Locate every blood parasite and identify its species.
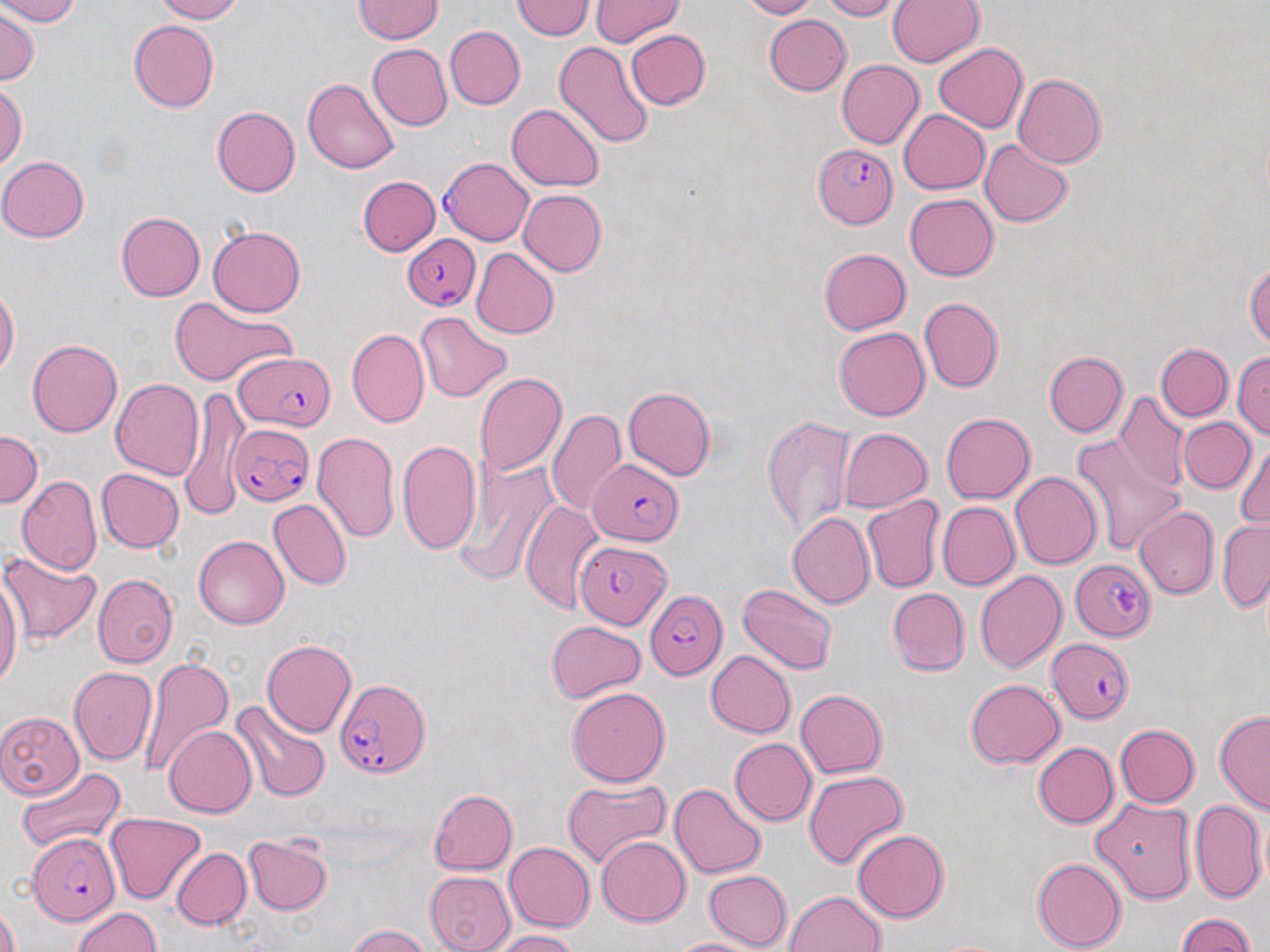

Approximate bounding boxes as named x1/y1/x2/y2 corners in pixels.
Plasmodium falciparum-infected red blood cells: (x1=813, y1=140, x2=898, y2=231), (x1=439, y1=157, x2=533, y2=247), (x1=401, y1=231, x2=481, y2=312), (x1=232, y1=350, x2=339, y2=432), (x1=230, y1=422, x2=314, y2=505), (x1=587, y1=460, x2=683, y2=544), (x1=576, y1=533, x2=680, y2=631), (x1=1070, y1=559, x2=1156, y2=640), (x1=648, y1=589, x2=727, y2=680), (x1=1046, y1=637, x2=1134, y2=725), (x1=339, y1=674, x2=433, y2=779), (x1=26, y1=831, x2=119, y2=925).
No Plasmodium ovale, Plasmodium malariae, Plasmodium vivax, Babesia divergens, or Trypanosoma brucei observed.

Summary:
  - Uninfected red blood cell locations: (x1=0, y1=0, x2=84, y2=27), (x1=151, y1=0, x2=249, y2=23), (x1=354, y1=0, x2=443, y2=44), (x1=592, y1=0, x2=683, y2=46), (x1=738, y1=0, x2=820, y2=18), (x1=819, y1=0, x2=899, y2=20), (x1=888, y1=0, x2=985, y2=68), (x1=511, y1=1, x2=593, y2=41), (x1=0, y1=8, x2=40, y2=85), (x1=764, y1=14, x2=851, y2=96), (x1=128, y1=20, x2=219, y2=111), (x1=444, y1=26, x2=526, y2=109), (x1=625, y1=29, x2=711, y2=110), (x1=550, y1=40, x2=655, y2=149), (x1=366, y1=43, x2=451, y2=131), (x1=932, y1=43, x2=1029, y2=133), (x1=835, y1=60, x2=925, y2=149), (x1=1011, y1=74, x2=1105, y2=168), (x1=302, y1=78, x2=399, y2=175), (x1=0, y1=83, x2=26, y2=171), (x1=507, y1=101, x2=605, y2=191), (x1=215, y1=106, x2=301, y2=198), (x1=897, y1=108, x2=990, y2=194), (x1=979, y1=139, x2=1072, y2=227), (x1=0, y1=154, x2=90, y2=243), (x1=359, y1=176, x2=439, y2=256), (x1=517, y1=189, x2=608, y2=277), (x1=905, y1=194, x2=999, y2=280), (x1=115, y1=212, x2=205, y2=301), (x1=208, y1=226, x2=307, y2=317), (x1=470, y1=247, x2=560, y2=340), (x1=818, y1=248, x2=911, y2=335), (x1=1245, y1=257, x2=1270, y2=351), (x1=0, y1=285, x2=18, y2=380), (x1=168, y1=296, x2=295, y2=387), (x1=917, y1=297, x2=1003, y2=393), (x1=417, y1=313, x2=512, y2=400), (x1=834, y1=327, x2=930, y2=421), (x1=346, y1=328, x2=429, y2=428), (x1=28, y1=339, x2=122, y2=438), (x1=1157, y1=343, x2=1234, y2=422), (x1=1232, y1=348, x2=1270, y2=441), (x1=1044, y1=350, x2=1127, y2=436), (x1=473, y1=372, x2=565, y2=477), (x1=109, y1=377, x2=207, y2=480), (x1=622, y1=386, x2=716, y2=481), (x1=177, y1=391, x2=250, y2=519), (x1=1113, y1=391, x2=1190, y2=491), (x1=546, y1=406, x2=625, y2=516), (x1=941, y1=413, x2=1035, y2=505), (x1=761, y1=415, x2=856, y2=541), (x1=1178, y1=416, x2=1255, y2=492), (x1=837, y1=428, x2=930, y2=512), (x1=311, y1=429, x2=400, y2=547), (x1=0, y1=431, x2=42, y2=511), (x1=1073, y1=434, x2=1184, y2=556), (x1=397, y1=438, x2=482, y2=553), (x1=1233, y1=439, x2=1269, y2=533), (x1=454, y1=459, x2=563, y2=585), (x1=96, y1=469, x2=183, y2=553), (x1=1010, y1=471, x2=1102, y2=570), (x1=17, y1=473, x2=102, y2=572), (x1=860, y1=496, x2=944, y2=594), (x1=521, y1=499, x2=604, y2=617), (x1=267, y1=500, x2=351, y2=591), (x1=936, y1=502, x2=1019, y2=591), (x1=1135, y1=506, x2=1219, y2=600), (x1=787, y1=512, x2=874, y2=609), (x1=1217, y1=518, x2=1270, y2=614), (x1=193, y1=535, x2=289, y2=628), (x1=0, y1=546, x2=102, y2=644), (x1=0, y1=567, x2=22, y2=694), (x1=974, y1=570, x2=1065, y2=675), (x1=93, y1=574, x2=176, y2=665), (x1=735, y1=582, x2=838, y2=675), (x1=887, y1=588, x2=970, y2=675), (x1=546, y1=620, x2=645, y2=701), (x1=261, y1=638, x2=357, y2=738), (x1=706, y1=650, x2=796, y2=739), (x1=137, y1=656, x2=235, y2=779), (x1=69, y1=666, x2=156, y2=766), (x1=963, y1=678, x2=1063, y2=769), (x1=567, y1=685, x2=672, y2=786), (x1=795, y1=689, x2=889, y2=778), (x1=232, y1=700, x2=330, y2=802), (x1=0, y1=709, x2=83, y2=799), (x1=1214, y1=711, x2=1269, y2=811), (x1=164, y1=724, x2=257, y2=819), (x1=1114, y1=724, x2=1199, y2=807), (x1=728, y1=738, x2=814, y2=825), (x1=1032, y1=741, x2=1118, y2=829), (x1=15, y1=765, x2=127, y2=855), (x1=802, y1=769, x2=909, y2=872), (x1=562, y1=779, x2=673, y2=868), (x1=670, y1=783, x2=766, y2=879), (x1=426, y1=787, x2=518, y2=875), (x1=1090, y1=796, x2=1199, y2=900), (x1=1188, y1=796, x2=1266, y2=903), (x1=106, y1=811, x2=205, y2=904), (x1=851, y1=828, x2=947, y2=921), (x1=243, y1=835, x2=334, y2=917), (x1=596, y1=836, x2=689, y2=926), (x1=502, y1=842, x2=593, y2=932), (x1=173, y1=847, x2=251, y2=930), (x1=1031, y1=856, x2=1127, y2=950), (x1=705, y1=868, x2=791, y2=949), (x1=424, y1=870, x2=516, y2=952), (x1=784, y1=889, x2=888, y2=952), (x1=0, y1=906, x2=20, y2=952), (x1=70, y1=907, x2=165, y2=952), (x1=1172, y1=912, x2=1260, y2=951), (x1=347, y1=925, x2=433, y2=952), (x1=490, y1=929, x2=582, y2=952), (x1=670, y1=933, x2=762, y2=952)
  - Slide-level diagnosis: Plasmodium falciparum
  - Field of view: single
  - Preparation: thin blood smear
  - Magnification: 1000x
  - Modality: optical microscopy
  - Stain: May-Grünwald-Giemsa
  - Image size: 1270×952 pixels